State which parasite is depicted.
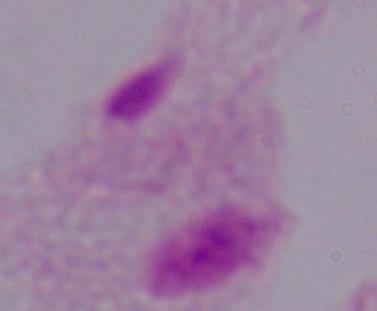

A trichomonad.

{
  "modality": "photomicrograph",
  "magnification": "1000x"
}